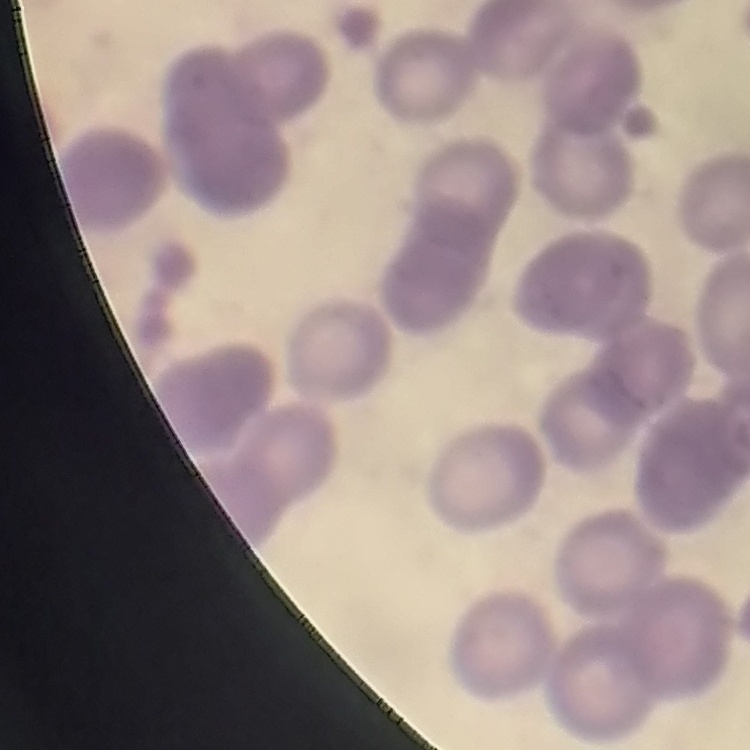

Summary:
  - Red blood cell morphology: rouleaux formation
  - Stain: Field's or Giemsa
  - Image type: one tile cut from a larger photomicrograph
  - Preparation: thin blood film